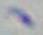

Summary:
  - Identification: Toxoplasma gondii
  - Magnification: 1000x
  - Modality: photomicrograph